Assess this cell for malaria.
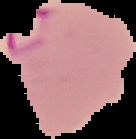

Parasitized.

Summary:
  - Image size: 136×139 pixels
  - Image type: segmented cell region on a black background
  - Preparation: thin blood smear